Give the position of every malaria parasite.
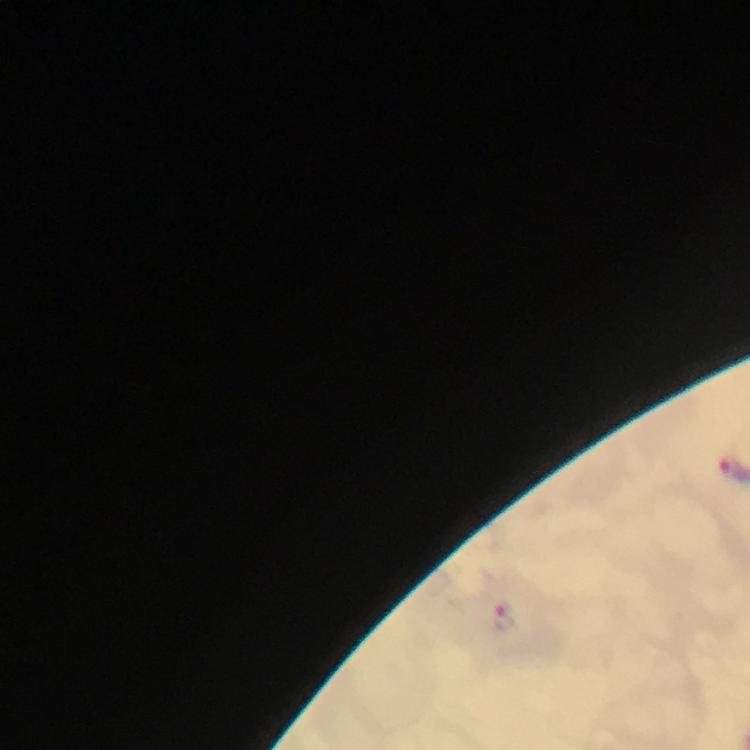
Approximate centers as [x, y] in pixels.
Malaria parasites: [507, 617].

Summary:
  - Preparation: thick smear
  - Context: from a malaria diagnostic workup
  - Magnification: 100x
  - Capture: smartphone photograph through a microscope
  - Image size: 750×750 pixels
  - Stain: Giemsa
  - Immersion oil: used
  - Cropped from: one field of view